Identify the parasite.
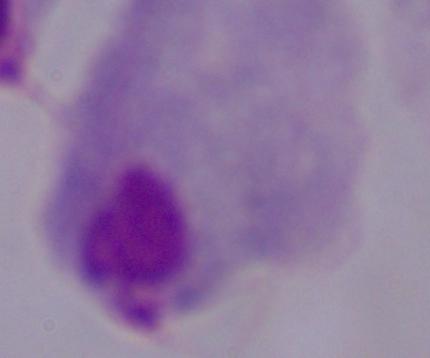
A trichomonad.

Summary:
  - Magnification: 1000x
  - Modality: photomicrograph